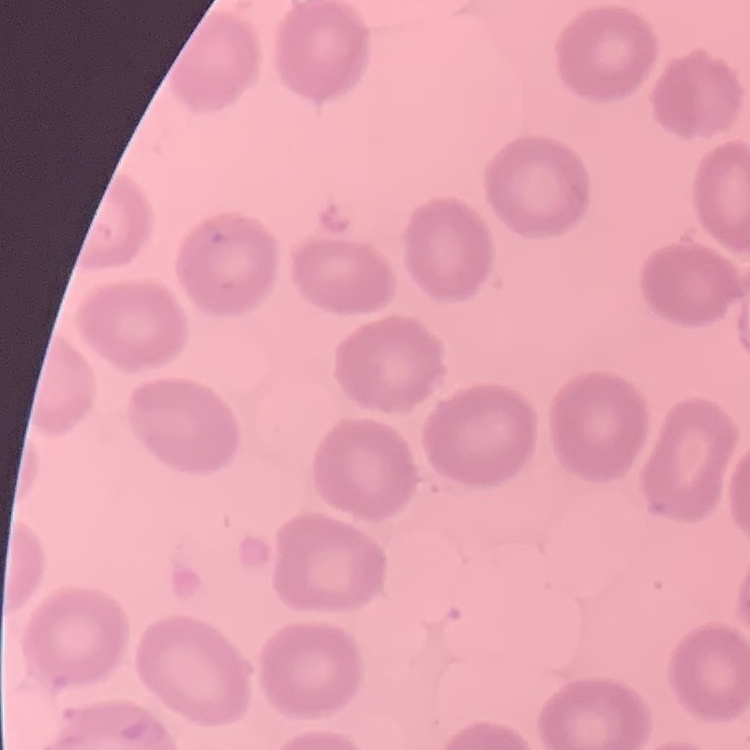

Summary:
  - Erythrocyte morphology: no rouleaux formation
  - Image type: square crop of a larger photomicrograph
  - Stain: Field's or Giemsa
  - Preparation: thin blood smear